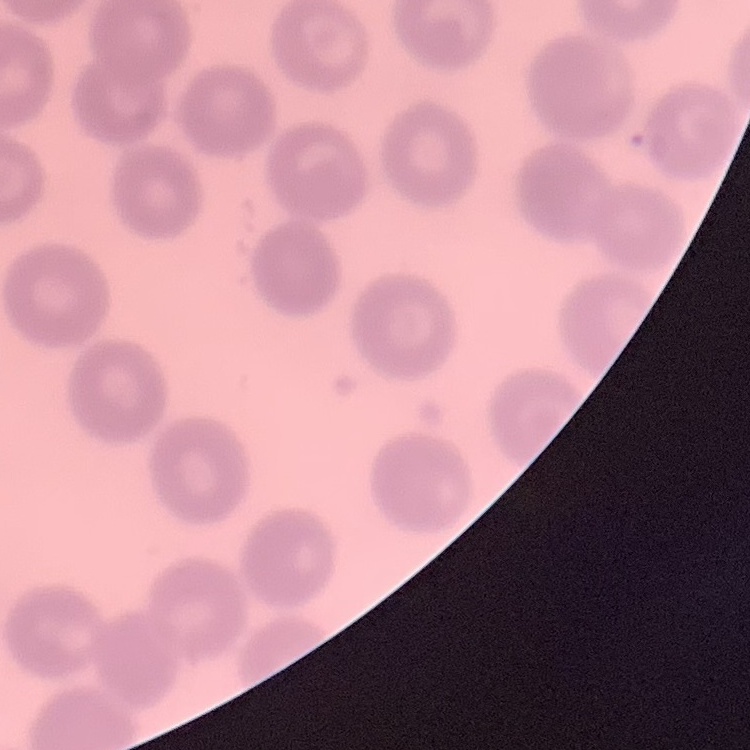
Summary:
  - Erythrocyte morphology: no rouleaux formation
  - Image type: one tile cut from a larger photomicrograph
  - Preparation: thin blood smear
  - Stain: Field's or Giemsa